Describe the morphology of the erythrocytes.
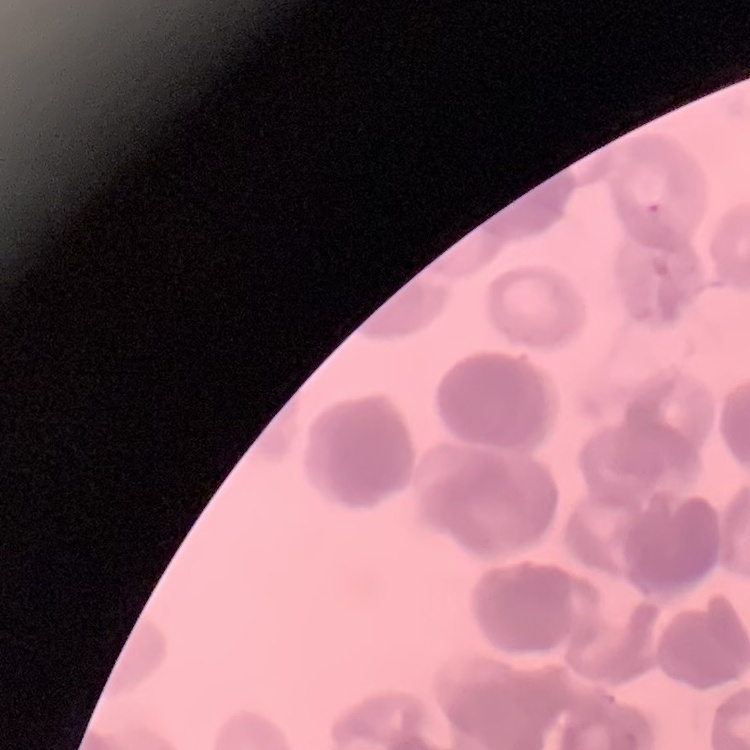
Rouleaux formation.

{
  "image_type": "square crop of a larger photomicrograph",
  "preparation": "thin peripheral smear",
  "stain": "Field's or Giemsa"
}